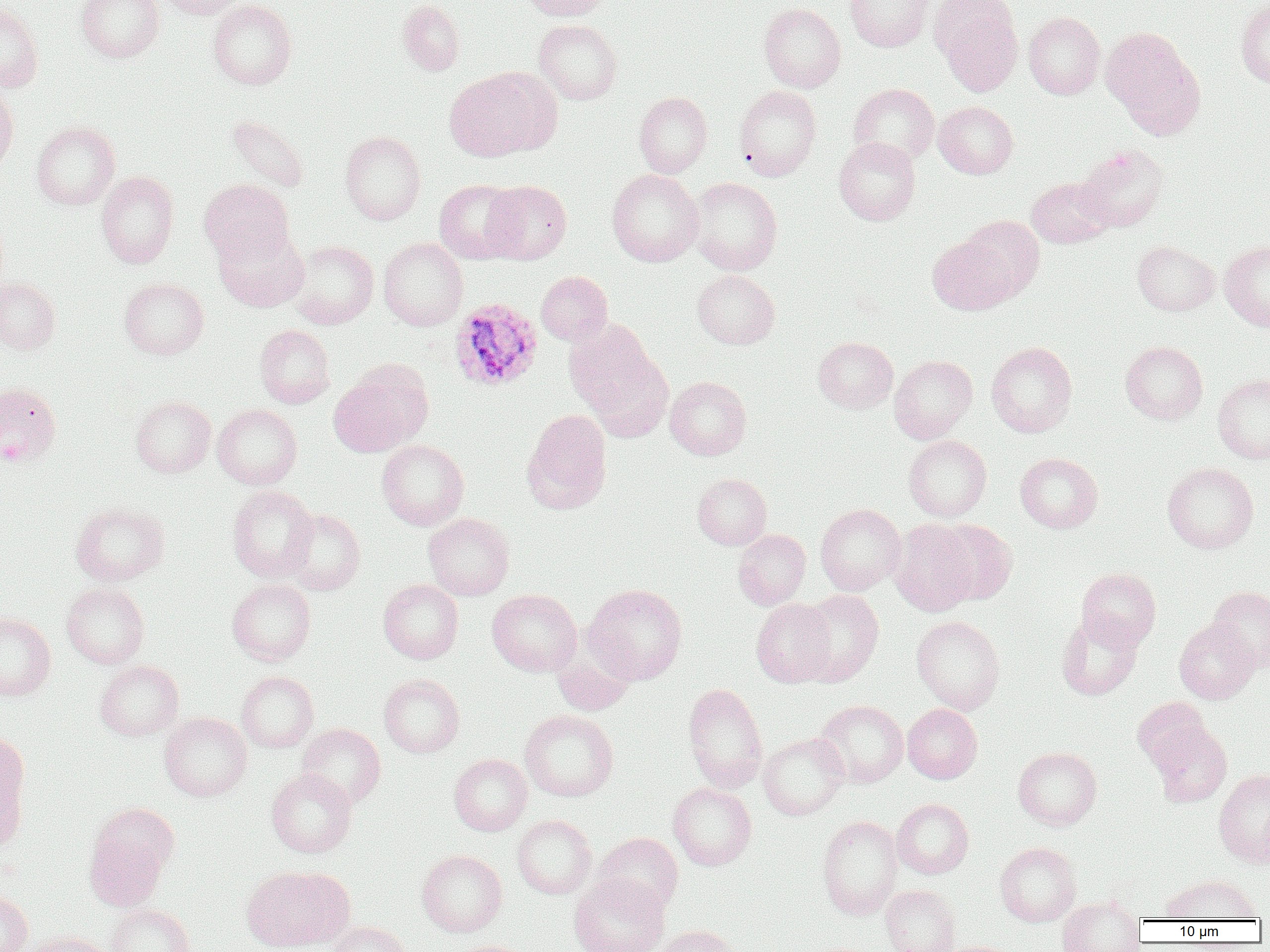 Approximate bounding boxes as (x1, y1, x2, y2) in pixels. Uninfected red blood cell locations: (76, 0, 164, 62), (156, 0, 247, 19), (208, 0, 297, 90), (397, 0, 464, 75), (519, 0, 611, 20), (845, 0, 934, 52), (1236, 0, 1270, 89), (0, 3, 44, 92), (758, 3, 845, 93), (934, 3, 1022, 96), (1024, 11, 1105, 99), (533, 19, 622, 104), (1100, 27, 1204, 137), (444, 70, 548, 160), (0, 83, 18, 176), (848, 83, 939, 166), (734, 85, 821, 181), (634, 92, 712, 177), (933, 101, 1018, 178), (226, 115, 310, 193), (31, 121, 120, 209), (340, 131, 426, 224), (834, 137, 920, 225), (1077, 144, 1168, 231), (607, 169, 704, 267), (96, 171, 179, 268), (689, 177, 782, 274), (1026, 177, 1115, 248), (199, 178, 294, 264), (433, 180, 523, 264), (483, 180, 572, 264), (960, 215, 1044, 299), (213, 226, 309, 312), (927, 235, 1016, 315), (378, 238, 468, 330), (289, 240, 378, 329), (1132, 240, 1219, 316), (1220, 240, 1270, 332), (692, 270, 780, 349), (536, 271, 612, 345), (0, 277, 60, 354), (119, 278, 208, 359), (565, 320, 666, 433), (255, 325, 335, 408), (813, 336, 898, 413), (986, 341, 1077, 437), (1120, 341, 1208, 424), (889, 352, 1078, 438), (889, 354, 978, 443), (330, 362, 431, 457), (1212, 373, 1270, 464), (665, 377, 751, 459), (0, 381, 61, 466), (131, 395, 215, 478), (213, 404, 302, 489), (522, 409, 612, 512), (904, 435, 991, 521), (377, 440, 469, 530), (1015, 452, 1103, 533), (1162, 462, 1258, 554), (692, 473, 772, 549), (228, 485, 317, 581), (70, 502, 170, 585), (815, 504, 906, 594), (281, 509, 365, 595), (424, 513, 514, 600), (890, 519, 978, 616), (932, 519, 1017, 604), (733, 530, 810, 609), (1076, 568, 1161, 649), (227, 579, 316, 665), (378, 579, 463, 664), (61, 582, 150, 668), (584, 584, 687, 684), (1208, 586, 1270, 672), (487, 589, 582, 676), (798, 589, 884, 686), (751, 598, 836, 687), (0, 611, 56, 701), (1056, 612, 1143, 700), (912, 615, 1004, 714), (1174, 619, 1260, 703), (552, 651, 634, 716), (95, 660, 183, 741), (236, 671, 319, 752), (379, 673, 465, 757), (683, 683, 768, 792), (1132, 697, 1214, 771), (815, 700, 908, 787), (902, 704, 982, 783), (520, 709, 618, 801), (159, 712, 251, 801), (1148, 721, 1232, 807), (297, 723, 385, 807), (0, 730, 30, 847), (758, 733, 849, 820), (1013, 747, 1102, 829), (449, 753, 532, 835), (265, 768, 358, 858), (1214, 769, 1270, 866), (668, 782, 756, 870), (892, 798, 973, 878), (817, 814, 902, 919), (512, 815, 596, 898), (83, 822, 171, 912), (592, 832, 682, 916), (995, 842, 1081, 926), (416, 849, 507, 937), (241, 866, 352, 952), (569, 873, 669, 952), (1162, 874, 1260, 921), (880, 884, 960, 952), (0, 889, 32, 952), (1057, 898, 1145, 952), (106, 903, 195, 952), (326, 921, 412, 952), (656, 925, 739, 952), (22, 932, 114, 952), (446, 940, 535, 952). Plasmodium ovale-infected red blood cell locations: (449, 297, 543, 391). Slide-level diagnosis: Plasmodium ovale. Light microscopy. Thin blood smear. Single field of view. Captured at 1000x magnification. Image is 1270×952 pixels.